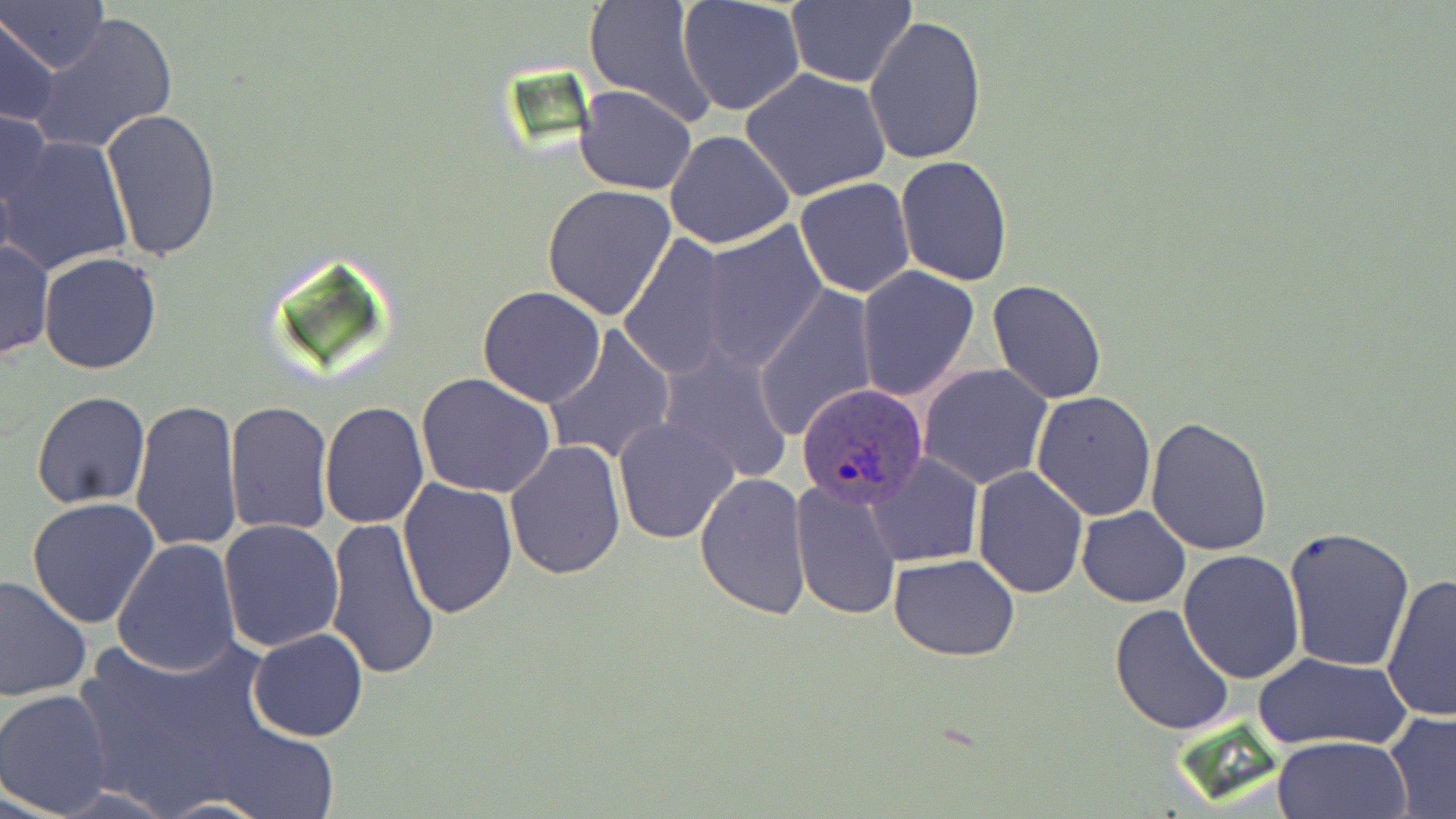

Approximate bounding boxes as [x1, y1, x2, y2] in pixels. Plasmodium ovale-infected red blood cell locations: [795, 382, 930, 509]. Uninfected red blood cell locations: [0, 0, 107, 73], [678, 0, 807, 118], [784, 1, 918, 88], [582, 2, 719, 126], [29, 11, 179, 155], [1, 12, 61, 127], [864, 15, 987, 165], [740, 67, 892, 201], [575, 85, 697, 195], [0, 103, 54, 236], [102, 107, 222, 263], [664, 129, 795, 249], [1, 135, 133, 275], [895, 156, 1013, 285], [794, 177, 917, 297], [541, 184, 676, 320], [699, 220, 830, 371], [617, 235, 736, 379], [0, 238, 54, 362], [39, 252, 163, 374], [856, 265, 980, 400], [988, 279, 1107, 404], [756, 286, 878, 440], [476, 287, 606, 408], [543, 324, 676, 466], [657, 348, 794, 484], [918, 364, 1053, 489], [416, 373, 555, 499], [1031, 390, 1157, 521], [32, 391, 151, 508], [130, 400, 243, 554], [223, 401, 335, 537], [318, 401, 428, 529], [613, 417, 739, 544], [1146, 418, 1274, 557], [505, 439, 627, 579], [866, 452, 982, 567], [971, 467, 1088, 596], [694, 470, 812, 619], [790, 477, 902, 621], [398, 478, 520, 618], [28, 496, 161, 629], [1076, 504, 1191, 607], [323, 517, 441, 681], [219, 519, 345, 653], [1282, 526, 1417, 672], [112, 537, 241, 675], [1178, 551, 1306, 684], [889, 554, 1021, 659], [1380, 574, 1456, 721], [0, 575, 92, 702], [1110, 604, 1237, 736], [71, 621, 303, 818], [247, 629, 369, 742], [1252, 651, 1412, 750], [0, 688, 117, 815], [1383, 710, 1456, 817], [1271, 734, 1411, 819], [155, 798, 267, 818]. Slide-level diagnosis: Plasmodium ovale. Captured at 1000x magnification. May-Grünwald-Giemsa stain. Optical microscopy. Thin blood film. Single field of view. Image is 1456×819 pixels.